Point out each Plasmodium parasite.
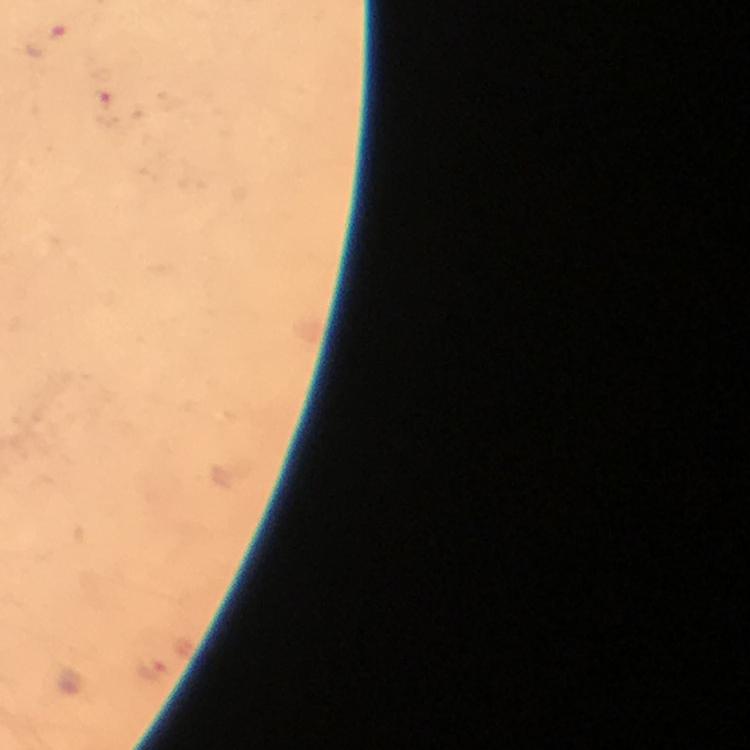

Approximate centers as (x, y) in pixels.
Plasmodium parasites: (107, 113), (148, 670).

magnification = 100x
cropped from = one field of view
stain = Giemsa
preparation = thick blood film
image size = 750×750 pixels
capture = smartphone camera through the microscope
context = from a malaria diagnostic workup
immersion oil = used